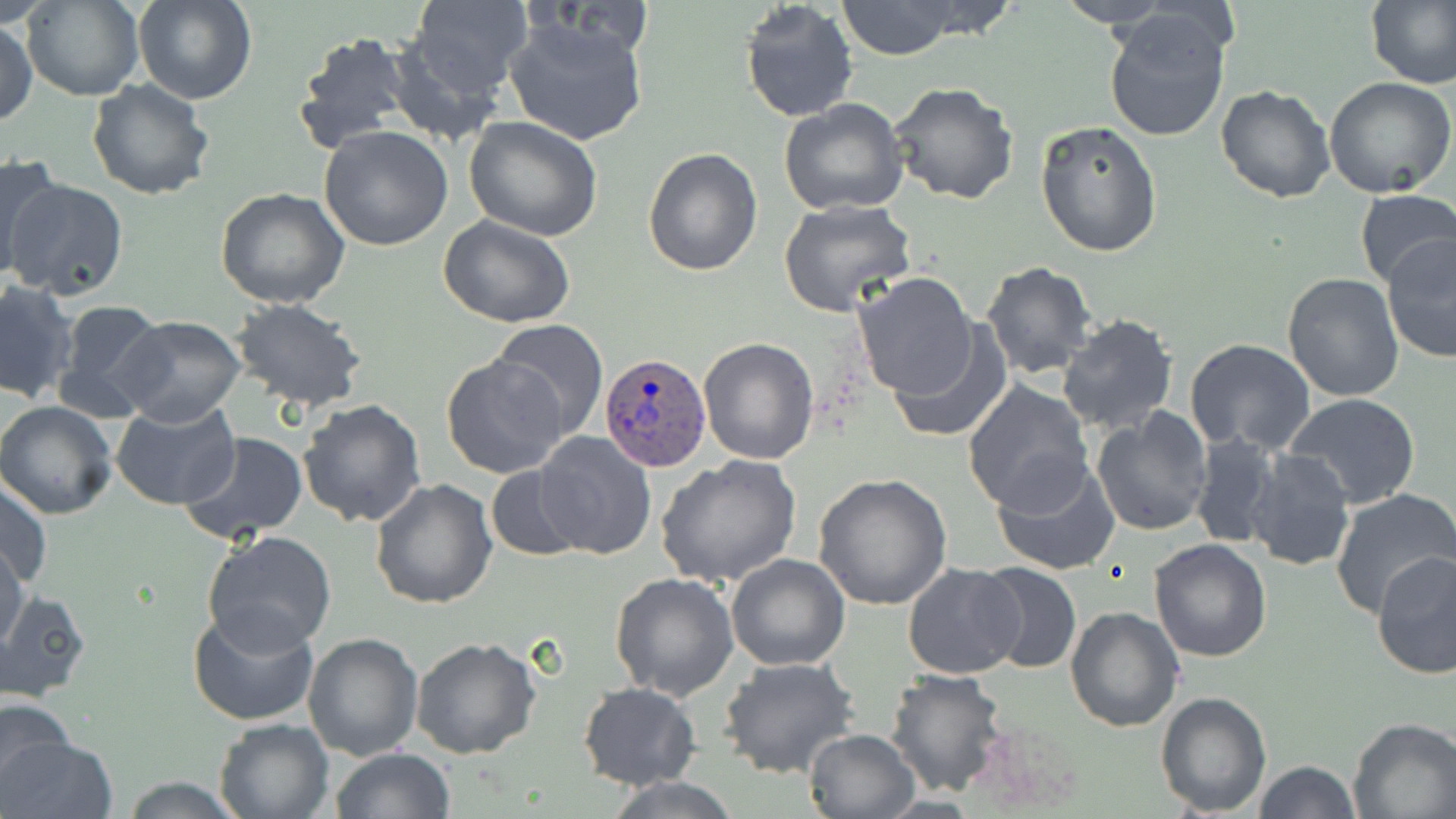
slide-level diagnosis = Plasmodium ovale
magnification = 1000x
field of view = one of a larger specimen
modality = optical microscopy
uninfected red blood cell locations = approximate bounding boxes as (x1,y1)-(x2,y2) corner pairs in pixels: (23,0)-(142,102), (132,0)-(257,106), (404,0)-(531,99), (835,0)-(963,59), (1054,0)-(1175,29), (1367,0)-(1456,91), (739,1)-(858,122), (1103,10)-(1234,141), (505,16)-(649,147), (0,19)-(37,126), (294,31)-(412,151), (384,33)-(508,147), (1325,77)-(1456,200), (85,79)-(216,202), (888,82)-(1019,204), (1215,85)-(1336,203), (778,98)-(909,218), (463,117)-(605,242), (1035,119)-(1164,256), (318,126)-(453,250), (643,148)-(763,276), (0,152)-(65,278), (6,178)-(130,299), (214,188)-(350,310), (1353,188)-(1456,292), (777,199)-(915,317), (438,215)-(577,328), (1380,232)-(1456,364), (979,260)-(1099,380), (852,272)-(976,399), (1280,273)-(1404,403), (0,281)-(80,405), (231,299)-(368,410), (52,301)-(170,420), (1057,314)-(1179,436), (115,315)-(246,425), (489,320)-(609,441), (886,321)-(1011,444), (697,337)-(820,466), (1185,338)-(1317,456), (440,354)-(571,481), (962,380)-(1095,513), (1284,393)-(1422,510), (298,398)-(427,527), (0,400)-(120,519), (110,401)-(239,511), (1091,408)-(1215,536), (531,431)-(657,560), (179,432)-(310,544), (1190,434)-(1280,550), (1244,450)-(1356,572), (654,455)-(802,585), (990,456)-(1120,576), (484,467)-(586,562), (812,475)-(954,611), (0,479)-(52,589), (370,479)-(498,609), (1329,488)-(1456,620), (202,531)-(338,652), (1148,538)-(1272,663), (0,539)-(29,655), (1372,550)-(1455,680), (725,554)-(851,672), (976,560)-(1082,673), (902,563)-(1024,679), (610,571)-(741,700), (0,590)-(92,701), (187,606)-(321,726), (1064,607)-(1184,733), (301,632)-(424,761), (411,636)-(542,759), (719,656)-(860,779), (884,669)-(1009,796), (577,683)-(701,790), (1154,690)-(1271,815), (0,697)-(79,800), (969,715)-(1090,814), (1347,717)-(1456,819), (213,718)-(336,818), (0,726)-(112,819), (802,727)-(918,818), (331,748)-(455,818), (1253,759)-(1360,818), (602,775)-(745,817), (116,776)-(248,818)
preparation = thin blood smear
Plasmodium ovale-infected red blood cell locations = approximate bounding boxes as (x1,y1)-(x2,y2) corner pairs in pixels: (599,354)-(713,469)
stain = May-Grünwald-Giemsa
image size = 1456×819 pixels